Name the blood parasite species.
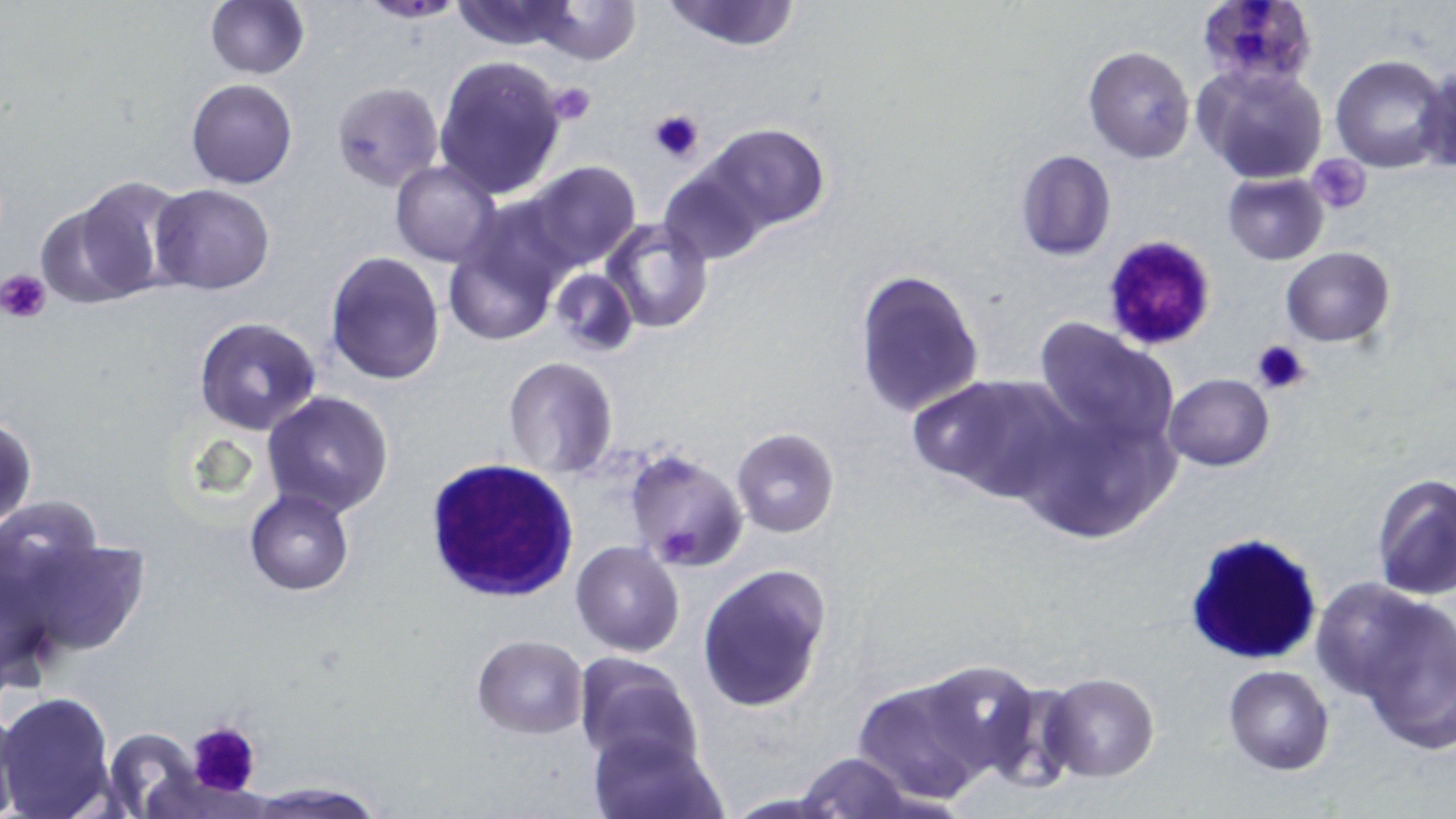
Plasmodium falciparum.

Summary:
  - Coordinate format: approximate bounding boxes as (x1, y1, x2, y2) in pixels
  - Plasmodium falciparum-infected red blood cell locations: (1194, 0, 1319, 95)
  - Uninfected red blood cell locations: (204, 0, 310, 80), (356, 0, 468, 23), (448, 0, 586, 52), (531, 0, 641, 66), (660, 0, 803, 50), (1083, 47, 1196, 163), (1330, 55, 1452, 174), (432, 56, 567, 200), (1418, 59, 1454, 174), (1197, 63, 1329, 186), (186, 79, 297, 189), (331, 81, 443, 192), (700, 123, 830, 235), (1013, 149, 1117, 261), (391, 161, 501, 268), (522, 162, 642, 271), (659, 164, 768, 265), (1222, 172, 1330, 265), (57, 177, 186, 303), (149, 184, 275, 295), (602, 215, 714, 333), (443, 234, 561, 347), (1281, 246, 1395, 346), (325, 252, 447, 386), (549, 268, 640, 358), (853, 268, 983, 417), (192, 316, 323, 436), (1033, 318, 1176, 448), (503, 356, 617, 477), (912, 373, 1073, 500), (1161, 373, 1274, 471), (262, 390, 394, 518), (1015, 398, 1181, 545), (1, 416, 36, 532), (730, 428, 839, 536), (623, 448, 750, 574), (1371, 474, 1455, 602), (245, 489, 353, 595), (7, 530, 151, 662), (569, 547, 684, 663), (697, 564, 831, 713), (1310, 577, 1440, 699), (1358, 602, 1455, 751), (472, 635, 589, 739), (573, 653, 703, 771), (908, 661, 1052, 790), (1223, 664, 1334, 775), (1040, 673, 1159, 782), (852, 674, 997, 804), (0, 690, 117, 818), (0, 707, 21, 818), (102, 727, 208, 817), (588, 729, 725, 819), (795, 752, 914, 819), (248, 778, 384, 816)
  - White blood cell locations: (424, 458, 581, 600), (1183, 531, 1326, 668)
  - Platelet locations: (545, 84, 596, 126), (648, 108, 705, 163), (1310, 155, 1371, 213), (1097, 232, 1216, 352), (2, 270, 52, 321), (1251, 339, 1312, 397), (187, 721, 262, 798)
  - Magnification: 1000x
  - Image size: 1456×819 pixels
  - Modality: optical microscopy
  - Field of view: single
  - Stain: May-Grünwald-Giemsa
  - Preparation: thin blood smear